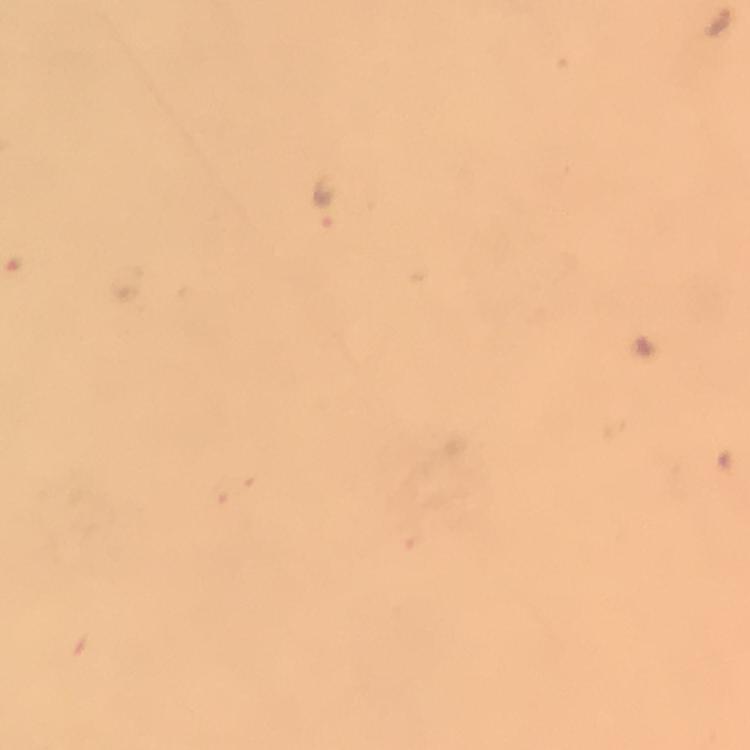

Approximate centers as (x, y) in pixels. Plasmodium parasite locations: (720, 20), (323, 203). From a diagnostic examination for malaria. Immersion oil was used. Photographed through the microscope with a smartphone camera. Thick blood film. A crop from one field of view. 100x magnification. Giemsa stain. Image is 750×750 pixels.